Assess the morphology of the erythrocytes.
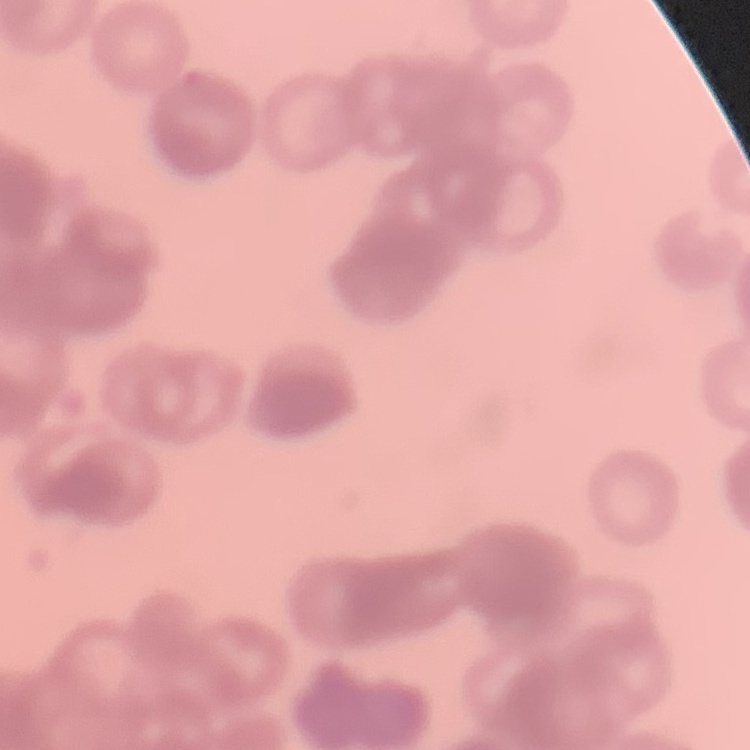
They show rouleaux formation.

One tile cut from a larger photomicrograph. Thin peripheral smear. Stained with either Field's or Giemsa.